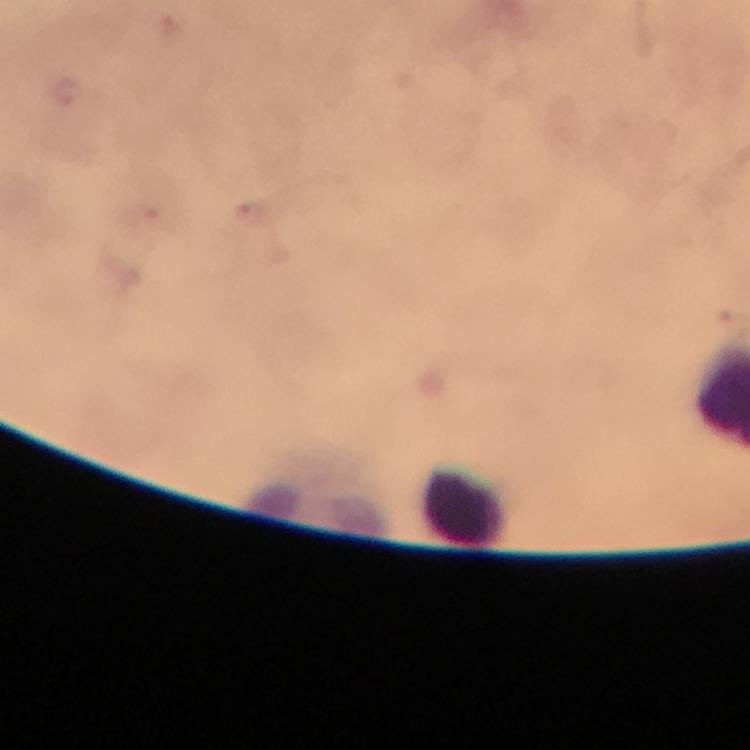

preparation: thick smear
malaria_parasites: none detected
leukocyte_locations: 'approximate object centers, in pixels from the top-left corner: (x=465, y=503)'
stain: Giemsa
magnification: 100x
context: from a malaria diagnostic workup
cropped_from: one field of view
immersion_oil: used
capture: smartphone photograph through a microscope
image_size: 750×750 pixels